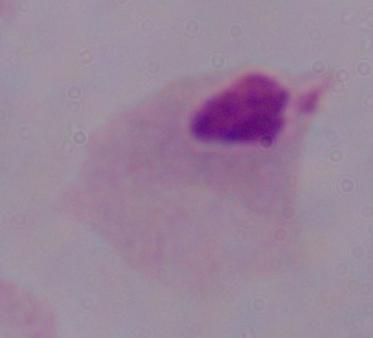

A trichomonad is shown. Captured at 1000x magnification. Photomicrograph.